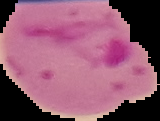 Cell region segmented out of the field of view; the surrounding area is masked to black. Image is 160×121 pixels. Malaria status: parasitized. From a thin blood film.